Assess the morphology of the erythrocytes.
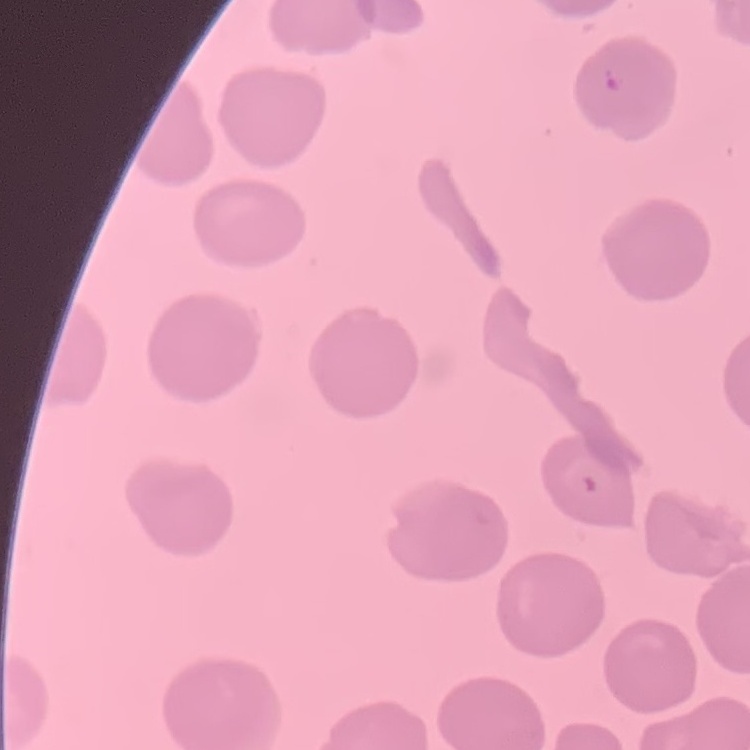
No rouleaux formation.

Summary:
  - Stain: Field's or Giemsa
  - Preparation: thin blood smear
  - Image type: one tile cut from a larger photomicrograph